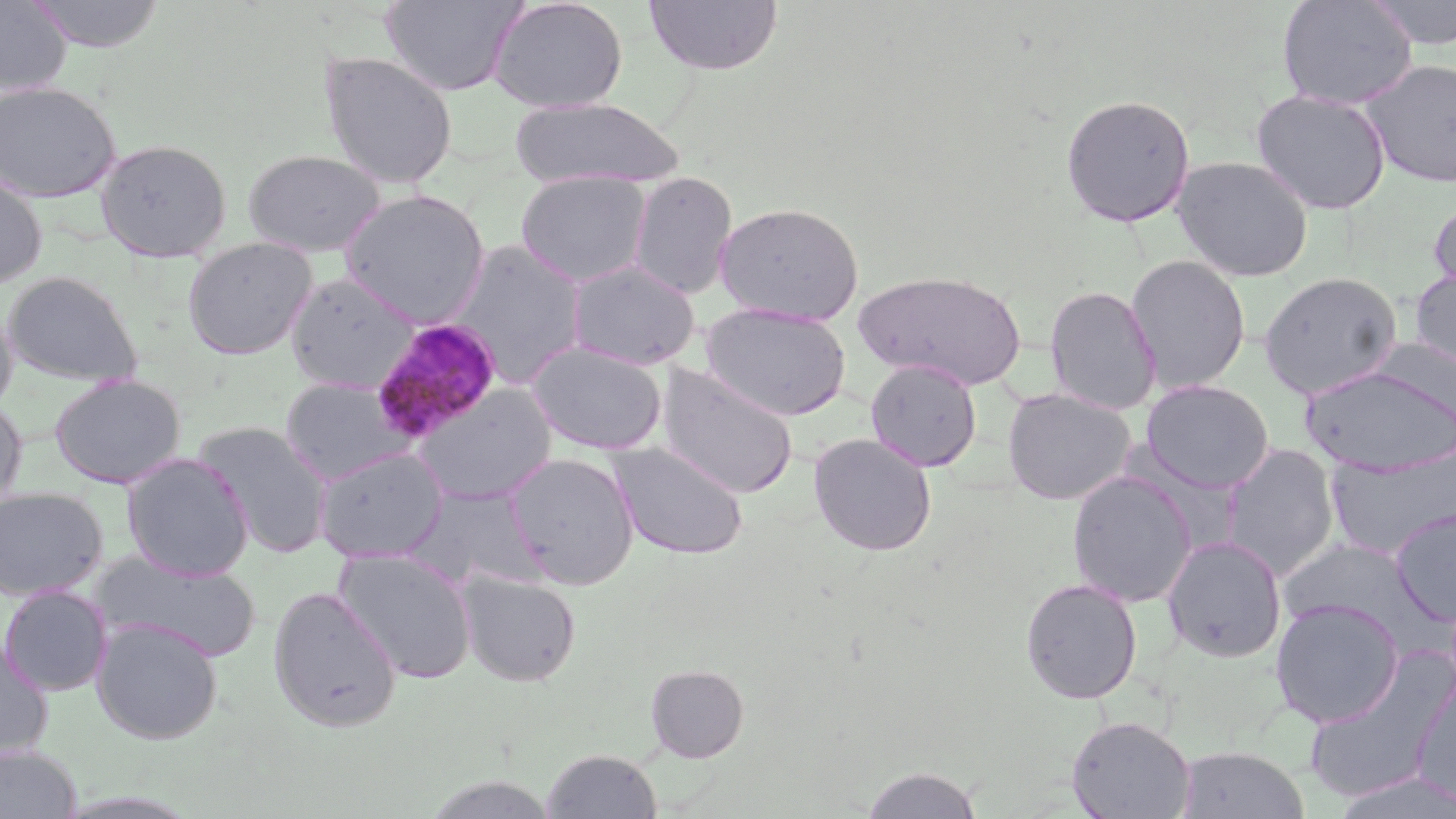

{
  "slide_level_diagnosis": "Plasmodium malariae",
  "uninfected_red_blood_cell_locations": "approximate bounding boxes as [x1, y1, x2, y2] in pixels: [25, 0, 167, 52], [380, 0, 526, 97], [488, 0, 627, 113], [642, 0, 784, 75], [1275, 0, 1418, 110], [1365, 0, 1456, 50], [0, 1, 72, 96], [318, 50, 458, 190], [1358, 58, 1456, 188], [0, 81, 121, 202], [1251, 89, 1392, 215], [1059, 93, 1195, 227], [510, 97, 686, 190], [96, 138, 231, 262], [243, 149, 386, 257], [1172, 155, 1314, 282], [0, 170, 47, 289], [515, 171, 651, 287], [628, 171, 737, 299], [339, 189, 491, 327], [1428, 195, 1456, 303], [714, 201, 864, 325], [183, 237, 318, 360], [447, 240, 588, 388], [1125, 255, 1251, 393], [567, 259, 699, 369], [1410, 267, 1456, 374], [853, 270, 1029, 390], [2, 271, 142, 387], [1258, 271, 1403, 399], [284, 272, 419, 393], [1044, 284, 1162, 415], [0, 300, 18, 418], [700, 302, 852, 421], [1371, 335, 1456, 438], [527, 342, 667, 455], [865, 358, 982, 472], [656, 364, 799, 500], [1299, 364, 1456, 476], [49, 373, 186, 489], [280, 377, 414, 485], [1141, 380, 1274, 493], [413, 383, 556, 504], [1002, 387, 1136, 506], [0, 396, 27, 516], [194, 421, 334, 557], [808, 433, 937, 556], [609, 440, 749, 560], [1324, 442, 1456, 560], [1221, 443, 1341, 580], [313, 448, 448, 562], [505, 451, 640, 590], [121, 453, 254, 581], [1066, 471, 1197, 607], [406, 484, 547, 593], [0, 486, 108, 601], [1389, 508, 1456, 626], [1162, 535, 1287, 663], [1278, 536, 1436, 642], [333, 548, 477, 684], [95, 552, 262, 663], [458, 571, 582, 687], [1020, 577, 1143, 704], [0, 585, 113, 696], [268, 585, 401, 733], [1270, 598, 1405, 727], [91, 617, 223, 745], [0, 636, 54, 762], [1301, 662, 1453, 804], [645, 663, 749, 762], [1411, 671, 1456, 806], [1066, 715, 1196, 819], [0, 744, 82, 819], [1176, 745, 1309, 819], [541, 748, 662, 818], [860, 765, 984, 818], [1328, 771, 1456, 819]",
  "field_of_view": "single",
  "stain": "May-Grünwald-Giemsa",
  "preparation": "thin blood smear",
  "magnification": "1000x",
  "plasmodium_malariae_infected_red_blood_cell_locations": "approximate bounding boxes as [x1, y1, x2, y2] in pixels: [369, 319, 501, 443]",
  "modality": "light microscopy",
  "image_size": "1456×819 pixels"
}